Classify this cell by malaria status.
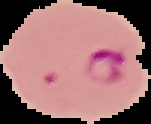

It is parasitized.

Segmented cell region on a black background. From a thin blood film. Image is 151×124 pixels.